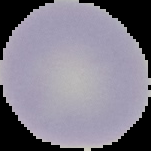

preparation = thin blood smear
image size = 151×151 pixels
image type = segmented cell region with the area outside set to black
malaria status = uninfected